Give the position of every malaria parasite.
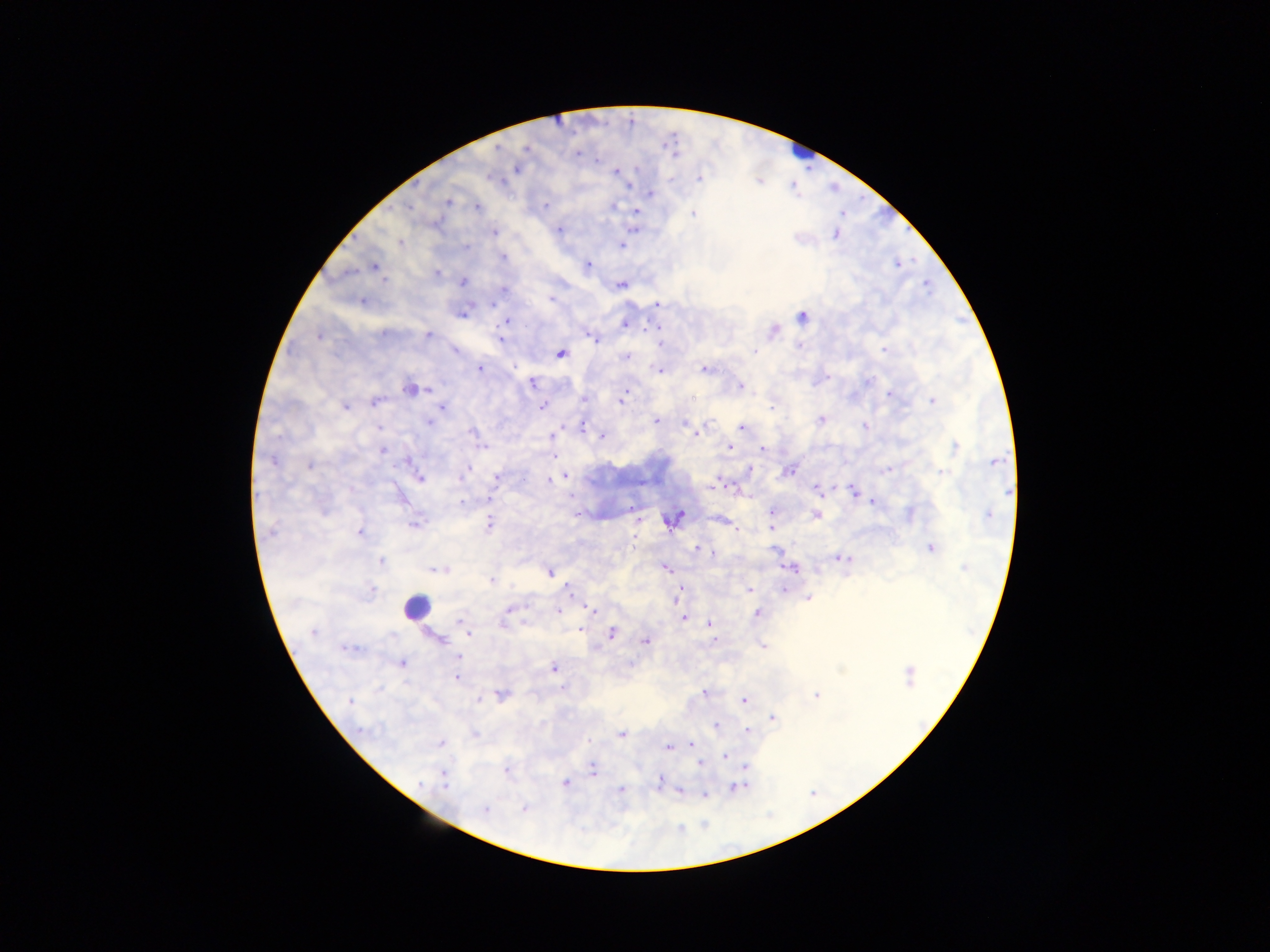

Approximate centers as (x, y) in pixels.
Malaria parasites: (576, 154), (597, 160), (517, 168), (616, 173), (671, 178), (700, 178), (650, 194), (448, 201), (545, 206), (613, 206), (409, 207), (477, 207), (636, 212), (693, 213), (436, 224), (558, 230), (493, 232), (835, 234), (401, 242), (621, 245), (466, 246), (502, 256), (588, 265), (374, 266), (437, 273), (383, 281), (463, 281), (621, 286), (504, 290), (550, 300), (362, 301), (657, 304), (463, 313), (802, 318), (506, 321), (625, 324), (656, 328), (773, 330), (383, 334), (429, 335), (319, 336), (592, 337), (500, 338), (660, 343), (798, 347), (886, 349), (455, 350), (755, 351), (560, 353), (625, 356), (480, 368), (704, 369), (659, 370), (828, 377), (868, 381), (531, 383), (741, 386), (408, 389), (427, 390), (889, 394), (623, 397), (584, 399), (621, 400), (933, 401), (375, 402), (441, 406), (543, 406), (345, 407), (772, 407), (821, 419), (655, 421), (429, 422), (687, 423), (865, 426), (378, 428), (582, 428), (690, 428), (742, 428), (472, 432), (697, 433), (552, 435), (601, 436), (729, 446), (955, 446), (483, 447), (762, 449), (383, 451), (554, 457), (272, 460), (408, 461), (995, 461), (309, 465), (749, 469), (889, 470), (787, 472), (942, 472), (466, 473), (566, 477), (419, 478), (460, 478), (497, 478), (554, 479), (550, 481), (714, 486), (817, 489), (854, 490), (1008, 491), (487, 499), (462, 502), (871, 502), (630, 507), (773, 511), (909, 514), (816, 515), (989, 515), (678, 516), (673, 520), (489, 523), (414, 525), (772, 527), (736, 528), (270, 533), (359, 533), (633, 542), (931, 548), (697, 549), (774, 550), (713, 553), (840, 558), (381, 562), (963, 568), (665, 569), (793, 569), (433, 570), (441, 570), (550, 573), (492, 581), (748, 589), (783, 589), (372, 590), (570, 591), (680, 591), (808, 598), (509, 610), (593, 610), (557, 611), (757, 613), (684, 617), (461, 622), (503, 623), (709, 624), (581, 630), (312, 633), (612, 633), (468, 634), (393, 635), (439, 639), (645, 641), (713, 641), (762, 647), (344, 649), (459, 657), (401, 664), (553, 669), (909, 676), (455, 677), (562, 688), (704, 692), (502, 695), (816, 696), (479, 699), (744, 700), (350, 701), (773, 718), (716, 725), (362, 731), (748, 731), (474, 734), (621, 734), (441, 743), (691, 744), (668, 747), (725, 755), (701, 764), (745, 767), (592, 770), (507, 771), (443, 774), (660, 780), (444, 783), (565, 783), (418, 785), (738, 787), (620, 790), (680, 792), (704, 795), (485, 809), (524, 809).

country = Ghana
leukocyte locations = approximate centers as (x, y) in pixels: (802, 151), (415, 607)
image size = 1270×952 pixels
capture = mobile-phone photograph through a microscope
field of view = single
preparation = thick blood smear